Assess this cell for malaria.
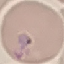

Parasitized.

image type = cell patch, automatically extracted from a larger field of view and resized to 64 × 64 pixels
capture = smartphone through the microscope eyepiece
stain = Giemsa
preparation = thin blood smear